Name the parasite shown.
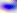
Toxoplasma gondii.

modality = photomicrograph
magnification = 400x